Comment on the morphology of the erythrocytes.
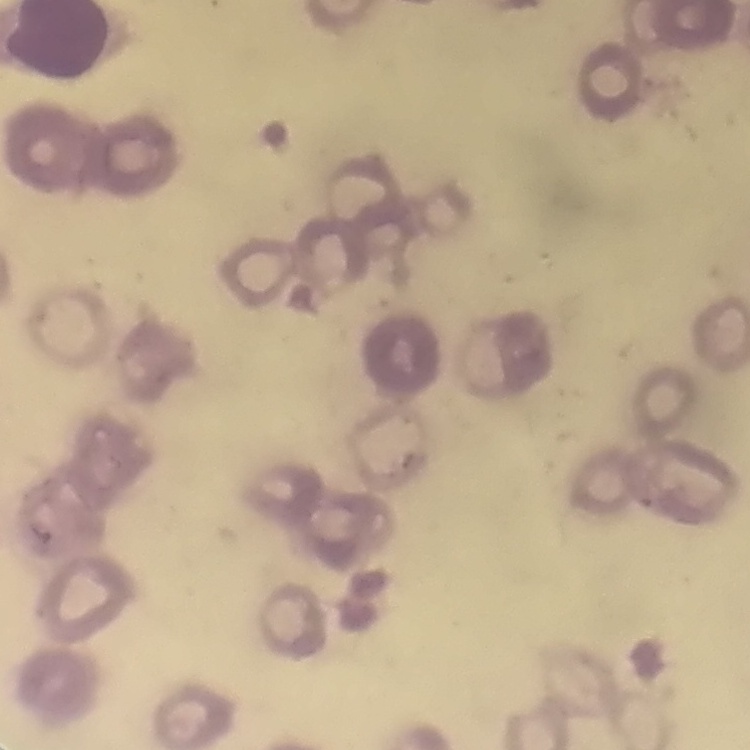
They show rouleaux formation.

One tile cut from a larger photomicrograph. Thin blood smear. Stained with either Field's or Giemsa.